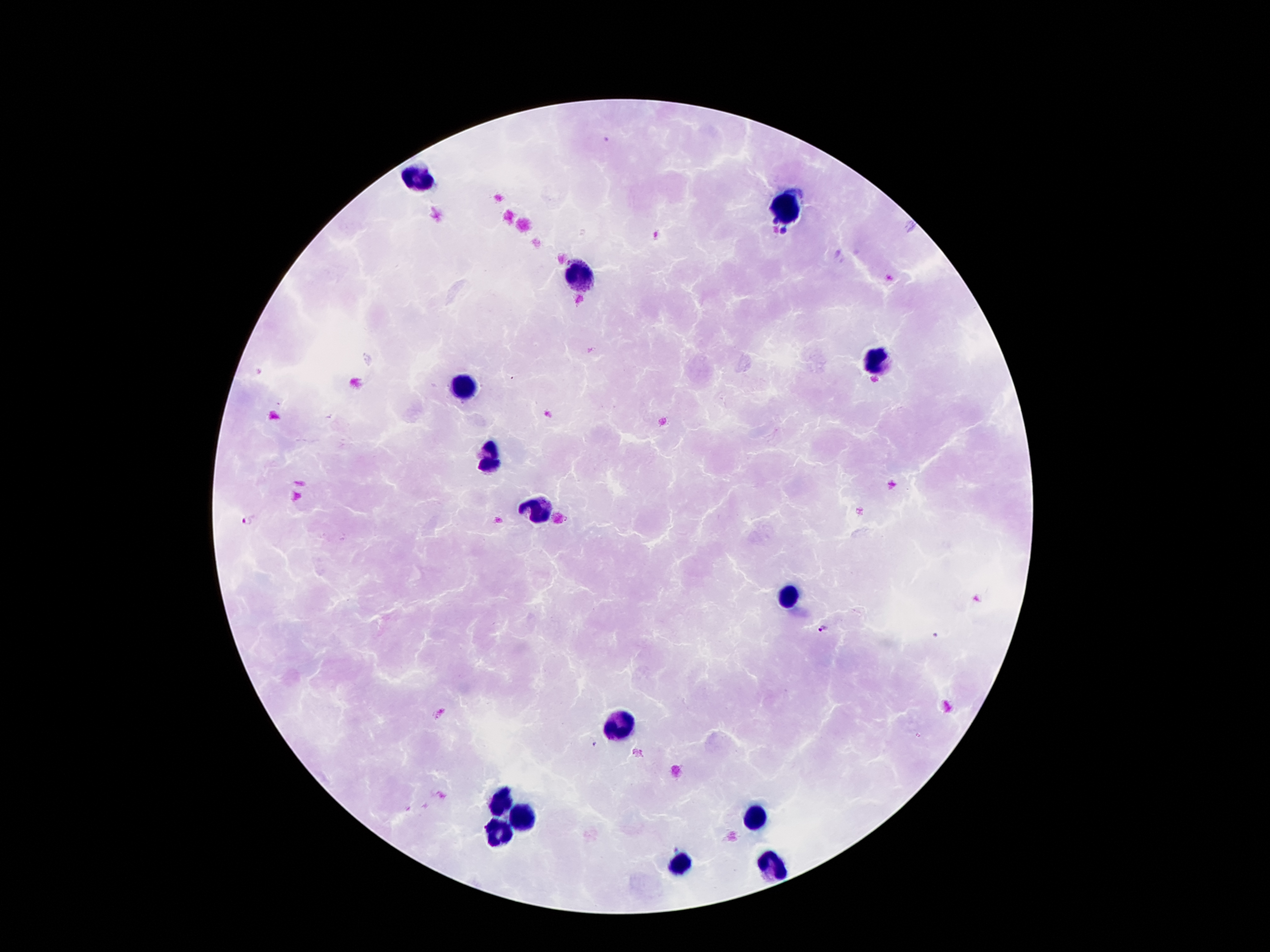
Approximate centers as (x, y) in pixels. Leukocyte locations: (416, 179), (787, 208), (577, 275), (878, 359), (464, 386), (491, 456), (537, 509), (786, 596), (616, 726), (502, 801), (520, 817), (755, 817), (495, 831), (683, 866), (770, 866). Malaria parasite locations: (249, 520), (824, 627), (935, 636), (595, 745). 100x magnification. Image is 1270×952 pixels. Patient malaria status: infected with Plasmodium falciparum. Giemsa stain. Single field of view. Smartphone photograph taken through the microscope eyepiece. Thick blood smear.